Outline each Plasmodium falciparum-infected red blood cell.
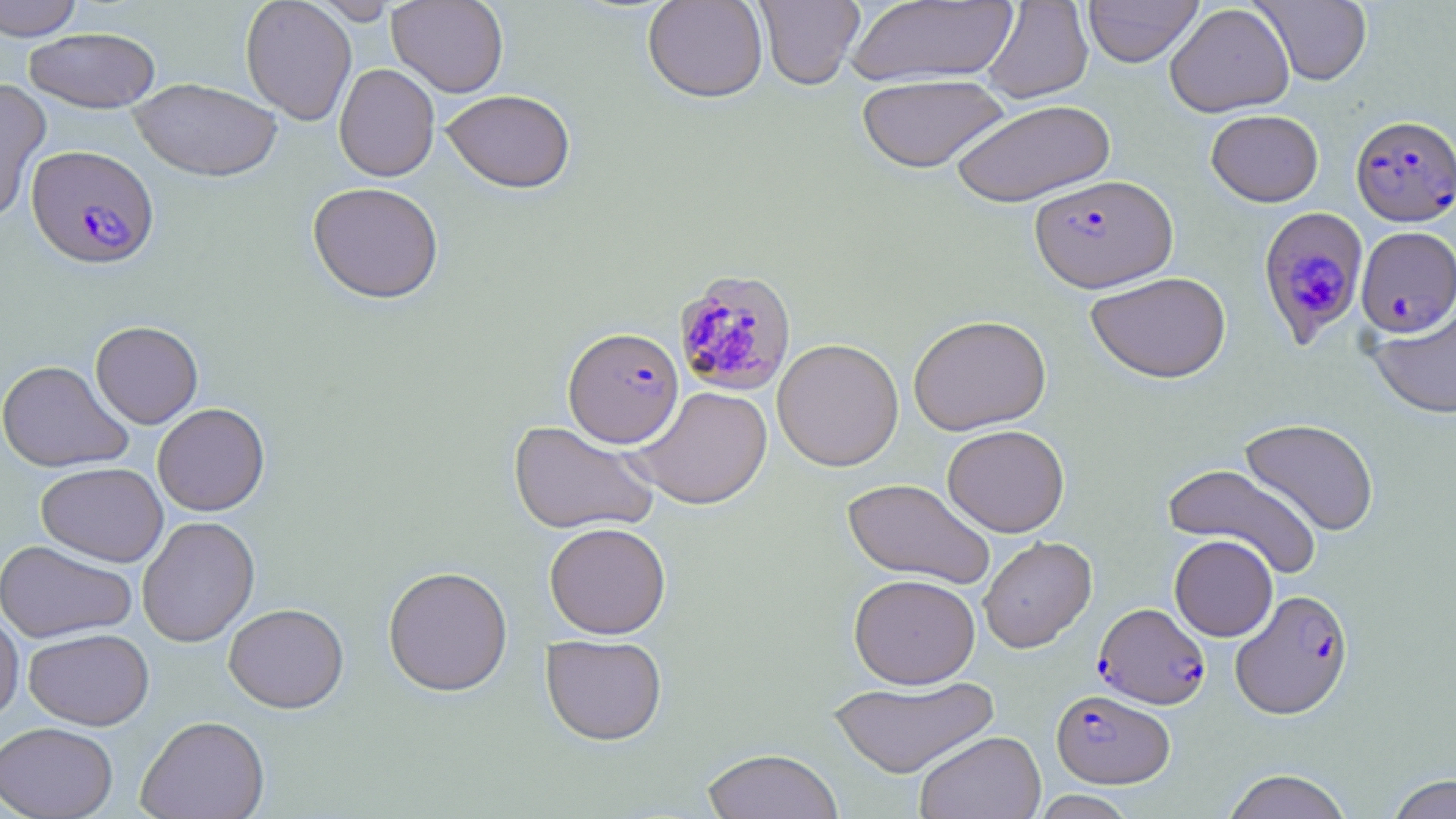

Approximate bounding boxes as (x1,y1)-(x2,y2) corner pairs in pixels.
Plasmodium falciparum-infected red blood cells: (1350,114)-(1456,225), (27,145)-(159,268), (1029,174)-(1178,292), (1258,207)-(1366,344), (1356,226)-(1456,338), (674,270)-(798,396), (563,326)-(684,448), (1230,589)-(1354,719), (1094,602)-(1210,709), (1051,688)-(1175,788).

Uninfected red blood cell locations: (0,0)-(84,40), (241,0)-(357,125), (311,0)-(400,24), (387,0)-(509,97), (642,0)-(767,103), (754,0)-(865,90), (846,0)-(1018,88), (1083,0)-(1202,67), (1251,0)-(1372,86), (982,1)-(1094,103), (1165,3)-(1294,117), (24,28)-(160,112), (334,63)-(439,182), (857,73)-(1008,173), (0,78)-(51,222), (130,78)-(282,181), (441,89)-(576,193), (950,98)-(1116,207), (1206,109)-(1323,207), (307,181)-(444,303), (1085,271)-(1232,384), (1366,305)-(1455,418), (908,315)-(1051,436), (90,320)-(203,428), (772,338)-(904,471), (0,360)-(133,473), (629,385)-(773,509), (153,402)-(270,516), (1239,418)-(1379,536), (507,420)-(661,535), (942,424)-(1070,537), (36,462)-(168,566), (1163,462)-(1321,579), (843,478)-(996,588), (137,515)-(259,647), (544,521)-(671,638), (1169,534)-(1278,641), (978,536)-(1096,653), (0,539)-(137,643), (383,565)-(513,696), (849,573)-(981,689), (223,603)-(349,713), (0,609)-(24,722), (24,627)-(154,730), (542,634)-(667,745), (827,676)-(999,778), (136,715)-(270,819), (0,721)-(118,819), (914,730)-(1045,819), (701,747)-(844,819), (1222,769)-(1353,819), (1386,774)-(1456,818), (1030,790)-(1138,819). Slide-level diagnosis: Plasmodium falciparum. Single field of view. Thin blood smear. May-Grünwald-Giemsa-stained preparation. Light microscopy. Image is 1456×819 pixels. Captured at 1000x magnification.